Give the extent of all Plasmodium vivax-infected red blood cells.
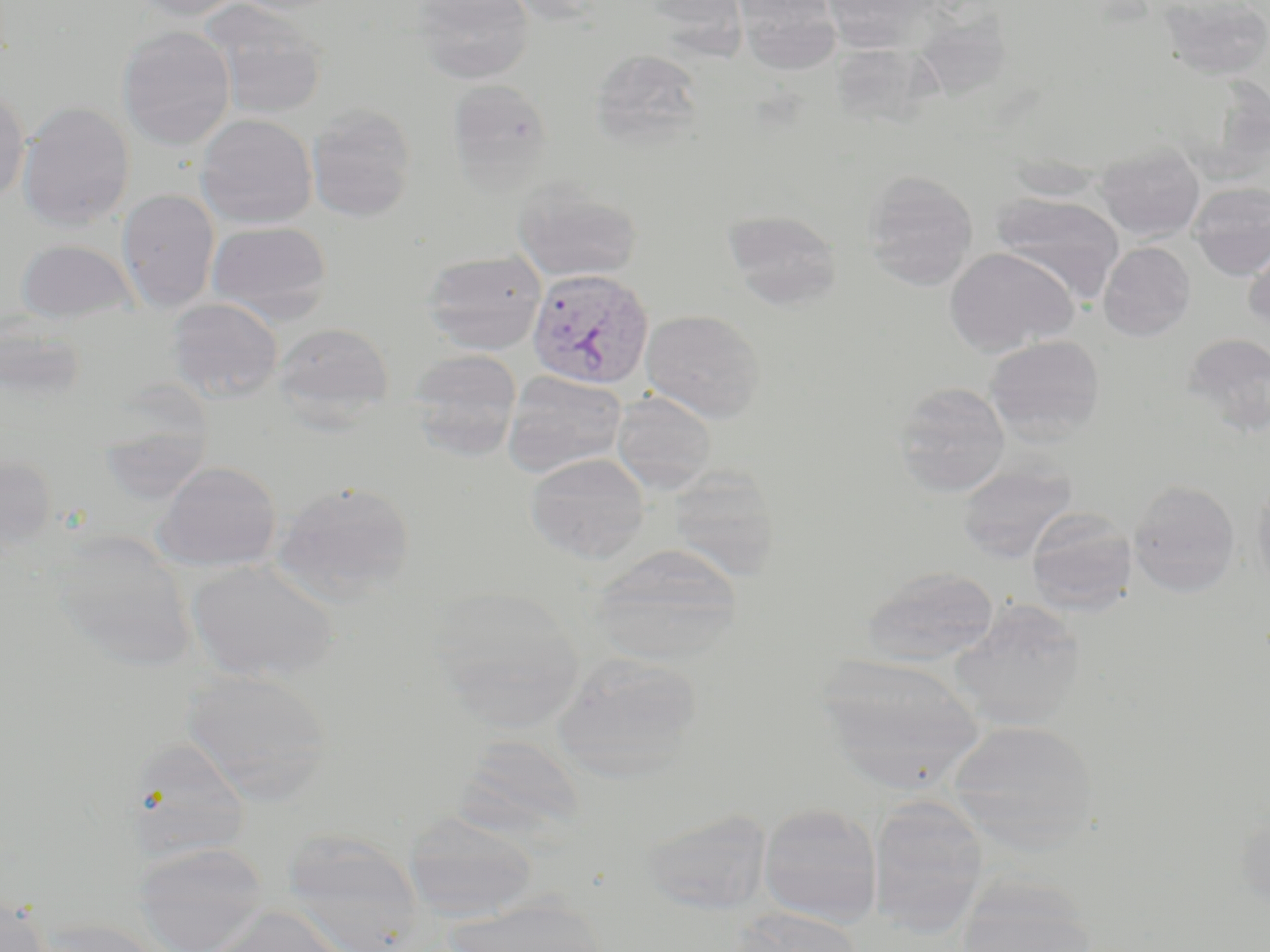

Approximate bounding boxes as (x1, y1, x2, y2) in pixels.
Plasmodium vivax-infected red blood cells: (527, 268, 656, 390).

{
  "slide_level_diagnosis": "Plasmodium vivax",
  "image_size": "1270×952 pixels",
  "modality": "light microscopy",
  "field_of_view": "one of a larger specimen",
  "magnification": "1000x",
  "uninfected_red_blood_cell_locations": "approximate bounding boxes as (x1, y1, x2, y2) in pixels: (128, 0, 247, 21), (199, 0, 329, 120), (411, 0, 535, 84), (639, 0, 747, 41), (736, 0, 841, 73), (1156, 0, 1270, 80), (822, 1, 937, 54), (117, 25, 235, 150), (589, 48, 706, 151), (445, 78, 554, 195), (0, 84, 30, 204), (17, 101, 135, 231), (305, 104, 418, 221), (195, 113, 318, 229), (1096, 141, 1205, 242), (860, 171, 979, 291), (512, 181, 643, 283), (1188, 182, 1270, 280), (116, 188, 221, 313), (990, 193, 1125, 304), (722, 209, 844, 310), (206, 220, 333, 323), (1243, 226, 1270, 332), (14, 239, 138, 325), (1098, 241, 1196, 341), (944, 247, 1079, 356), (419, 249, 548, 355), (166, 297, 284, 403), (641, 309, 766, 422), (0, 311, 87, 406), (272, 322, 394, 422), (1181, 333, 1270, 437), (984, 334, 1106, 444), (408, 350, 523, 460), (503, 371, 628, 477), (892, 381, 1011, 497), (611, 391, 717, 495), (96, 417, 215, 506), (525, 452, 651, 564), (0, 454, 57, 555), (955, 460, 1078, 563), (153, 461, 282, 572), (664, 466, 782, 582), (1251, 478, 1270, 597), (271, 479, 417, 605), (1128, 479, 1242, 598), (1026, 508, 1138, 615), (43, 529, 199, 672), (589, 544, 743, 666), (185, 559, 340, 683), (859, 566, 1001, 666), (424, 588, 587, 732), (949, 598, 1087, 732), (551, 652, 704, 783), (816, 654, 986, 794), (182, 668, 335, 804), (946, 719, 1100, 852), (454, 735, 586, 842), (123, 737, 252, 862), (867, 795, 990, 935), (758, 801, 883, 927), (1235, 805, 1270, 916), (640, 807, 773, 916), (403, 810, 539, 922), (280, 832, 425, 952), (132, 840, 268, 951), (953, 882, 1100, 952), (1, 892, 52, 952), (446, 897, 610, 952), (206, 906, 348, 952), (732, 906, 864, 952), (32, 917, 169, 952)",
  "stain": "May-Grünwald-Giemsa",
  "preparation": "thin blood smear"
}